Locate every malaria parasite.
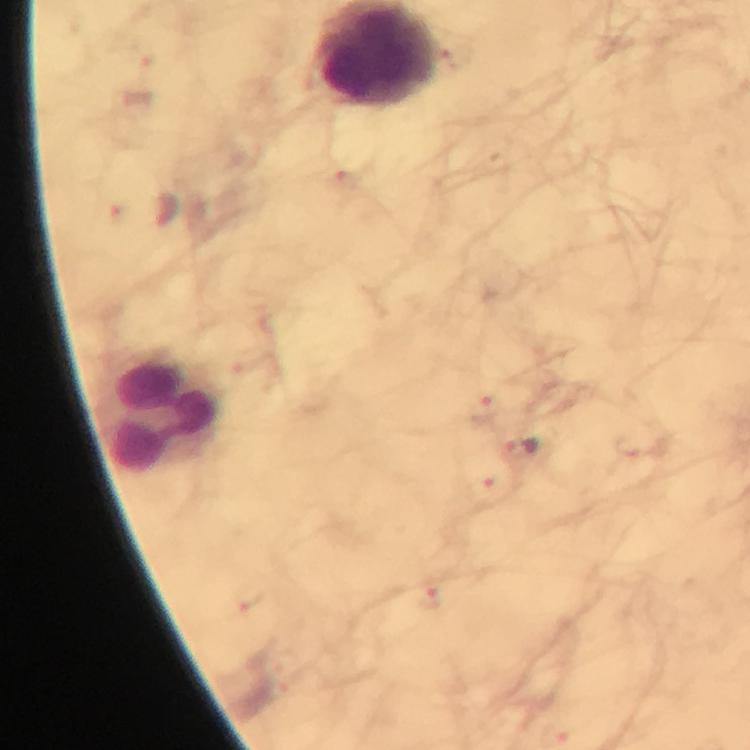
Approximate centers as (x, y) in pixels.
Malaria parasites: (483, 409), (521, 451), (483, 492), (249, 598), (429, 600).

Summary:
  - Leukocyte locations: (162, 411)
  - Capture: smartphone photograph through a microscope
  - Magnification: 100x
  - Context: from a malaria diagnostic workup
  - Preparation: thick blood smear
  - Stain: Giemsa
  - Immersion oil: applied
  - Cropped from: a single field of view
  - Image size: 750×750 pixels